Identify the blood parasite species.
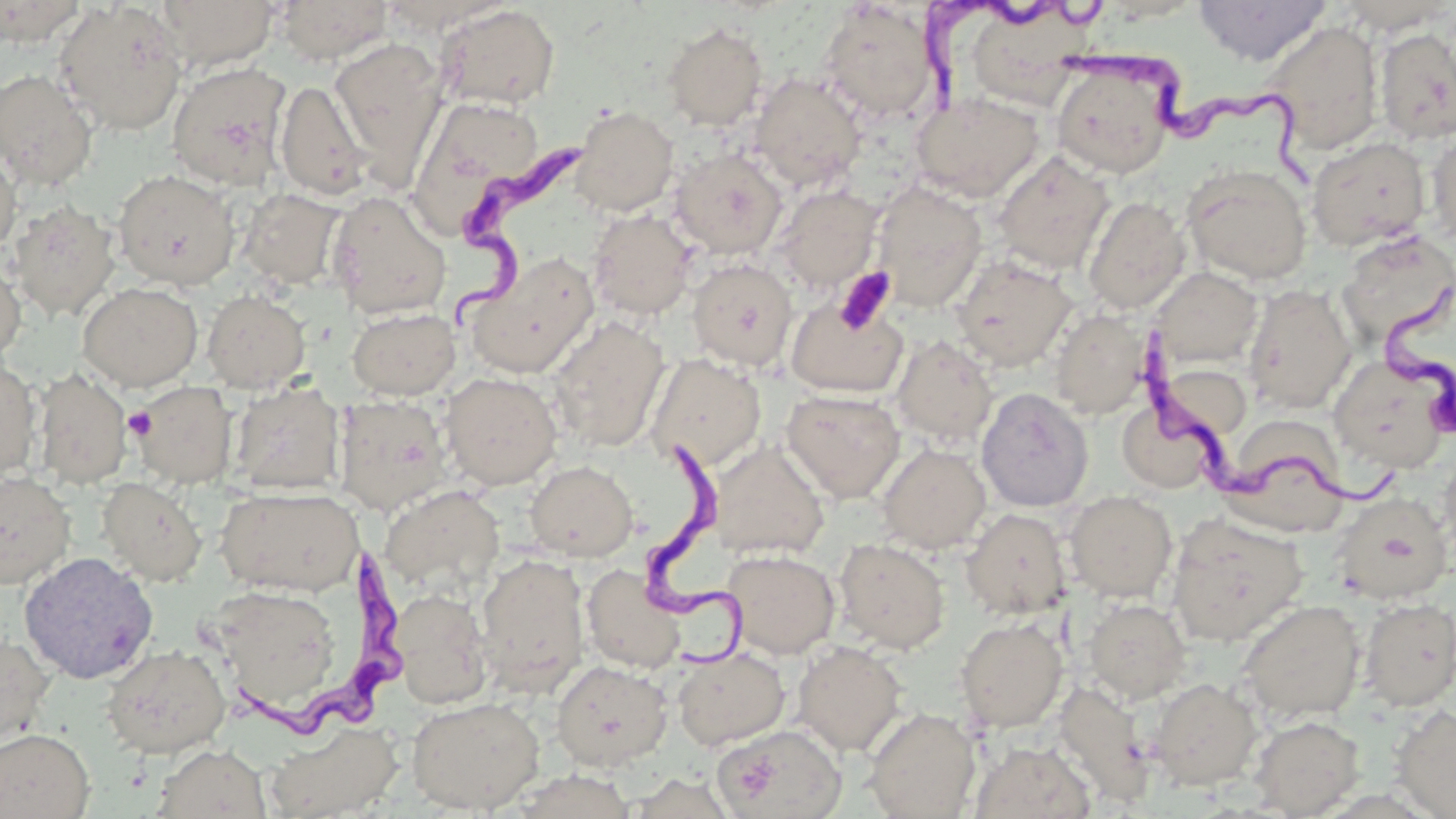

Trypanosoma brucei.

Summary:
  - Coordinate format: approximate bounding boxes as named x1/y1/x2/y2 corners in pixels
  - Trypanosoma brucei locations: (x1=905, y1=2, x2=1103, y2=133), (x1=1059, y1=31, x2=1329, y2=194), (x1=436, y1=132, x2=590, y2=333), (x1=1378, y1=278, x2=1453, y2=450), (x1=1133, y1=320, x2=1405, y2=517), (x1=639, y1=430, x2=748, y2=676), (x1=224, y1=548, x2=408, y2=753)
  - Uninfected red blood cell locations: (x1=54, y1=0, x2=188, y2=136), (x1=154, y1=0, x2=281, y2=71), (x1=275, y1=0, x2=393, y2=64), (x1=1193, y1=0, x2=1332, y2=66), (x1=0, y1=1, x2=88, y2=46), (x1=379, y1=1, x2=513, y2=35), (x1=1334, y1=1, x2=1454, y2=35), (x1=818, y1=3, x2=940, y2=123), (x1=436, y1=4, x2=560, y2=110), (x1=1262, y1=20, x2=1384, y2=154), (x1=662, y1=22, x2=768, y2=131), (x1=1375, y1=27, x2=1456, y2=145), (x1=329, y1=37, x2=448, y2=175), (x1=1051, y1=57, x2=1178, y2=178), (x1=167, y1=61, x2=292, y2=190), (x1=0, y1=69, x2=98, y2=192), (x1=750, y1=71, x2=867, y2=192), (x1=275, y1=80, x2=372, y2=200), (x1=910, y1=91, x2=1045, y2=203), (x1=408, y1=99, x2=550, y2=235), (x1=570, y1=105, x2=679, y2=217), (x1=1425, y1=131, x2=1456, y2=247), (x1=1306, y1=137, x2=1431, y2=251), (x1=670, y1=147, x2=788, y2=260), (x1=0, y1=151, x2=21, y2=256), (x1=993, y1=151, x2=1114, y2=274), (x1=1182, y1=164, x2=1312, y2=285), (x1=112, y1=169, x2=240, y2=289), (x1=871, y1=181, x2=988, y2=312), (x1=772, y1=184, x2=884, y2=293), (x1=237, y1=187, x2=347, y2=290), (x1=326, y1=189, x2=452, y2=320), (x1=1083, y1=196, x2=1190, y2=314), (x1=5, y1=200, x2=120, y2=321), (x1=588, y1=208, x2=697, y2=321), (x1=1337, y1=230, x2=1455, y2=347), (x1=466, y1=253, x2=600, y2=379), (x1=950, y1=254, x2=1078, y2=371), (x1=686, y1=257, x2=798, y2=371), (x1=0, y1=259, x2=26, y2=363), (x1=1151, y1=267, x2=1263, y2=369), (x1=77, y1=281, x2=202, y2=391), (x1=1243, y1=283, x2=1356, y2=414), (x1=202, y1=290, x2=310, y2=393), (x1=786, y1=294, x2=909, y2=398), (x1=347, y1=307, x2=460, y2=400), (x1=1050, y1=308, x2=1152, y2=419), (x1=548, y1=316, x2=671, y2=453), (x1=890, y1=334, x2=998, y2=447), (x1=647, y1=353, x2=767, y2=472), (x1=1329, y1=355, x2=1452, y2=473), (x1=0, y1=357, x2=41, y2=482), (x1=1157, y1=363, x2=1252, y2=442), (x1=32, y1=369, x2=133, y2=488), (x1=440, y1=372, x2=563, y2=490), (x1=230, y1=380, x2=345, y2=495), (x1=130, y1=381, x2=237, y2=488), (x1=976, y1=387, x2=1094, y2=512), (x1=781, y1=389, x2=906, y2=503), (x1=333, y1=395, x2=453, y2=515), (x1=1118, y1=397, x2=1222, y2=493), (x1=1223, y1=414, x2=1349, y2=525), (x1=709, y1=440, x2=830, y2=560), (x1=877, y1=443, x2=991, y2=554), (x1=1438, y1=448, x2=1456, y2=565), (x1=524, y1=460, x2=638, y2=561), (x1=0, y1=471, x2=76, y2=589), (x1=97, y1=477, x2=207, y2=586), (x1=381, y1=485, x2=505, y2=594), (x1=217, y1=487, x2=363, y2=596), (x1=1064, y1=490, x2=1177, y2=602), (x1=1332, y1=492, x2=1454, y2=604), (x1=961, y1=508, x2=1072, y2=620), (x1=1166, y1=513, x2=1308, y2=647), (x1=834, y1=537, x2=951, y2=654), (x1=722, y1=549, x2=840, y2=659), (x1=18, y1=551, x2=159, y2=685), (x1=475, y1=552, x2=590, y2=695), (x1=581, y1=564, x2=686, y2=674), (x1=209, y1=583, x2=344, y2=716), (x1=390, y1=588, x2=494, y2=709), (x1=1358, y1=597, x2=1456, y2=711), (x1=1084, y1=598, x2=1192, y2=704), (x1=1237, y1=599, x2=1366, y2=723), (x1=955, y1=618, x2=1069, y2=732), (x1=0, y1=630, x2=56, y2=748), (x1=793, y1=641, x2=907, y2=756), (x1=100, y1=643, x2=231, y2=758), (x1=671, y1=646, x2=791, y2=750), (x1=551, y1=660, x2=672, y2=771), (x1=1148, y1=677, x2=1262, y2=790), (x1=1052, y1=680, x2=1154, y2=807), (x1=406, y1=695, x2=546, y2=814), (x1=1390, y1=703, x2=1455, y2=818), (x1=862, y1=707, x2=981, y2=818), (x1=1249, y1=715, x2=1364, y2=818), (x1=265, y1=722, x2=403, y2=819), (x1=713, y1=723, x2=847, y2=819), (x1=0, y1=728, x2=95, y2=819), (x1=969, y1=741, x2=1096, y2=819), (x1=152, y1=744, x2=271, y2=819), (x1=504, y1=769, x2=640, y2=818), (x1=625, y1=772, x2=739, y2=818)
  - Platelet locations: (x1=834, y1=266, x2=897, y2=336), (x1=124, y1=407, x2=157, y2=441)
  - Field of view: one of a larger specimen
  - Image size: 1456×819 pixels
  - Stain: May-Grünwald-Giemsa
  - Preparation: thin blood film
  - Magnification: 1000x
  - Modality: light microscopy